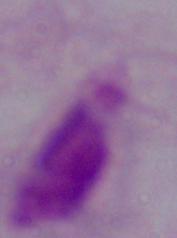

modality = photomicrograph
magnification = 1000x
identification = trichomonad